Assess this cell for malaria.
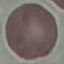

Uninfected.

Summary:
  - Preparation: thin blood smear
  - Capture: smartphone through the microscope eyepiece
  - Stain: Giemsa
  - Image type: cell patch, automatically extracted from a larger field of view and resized to 64 × 64 pixels